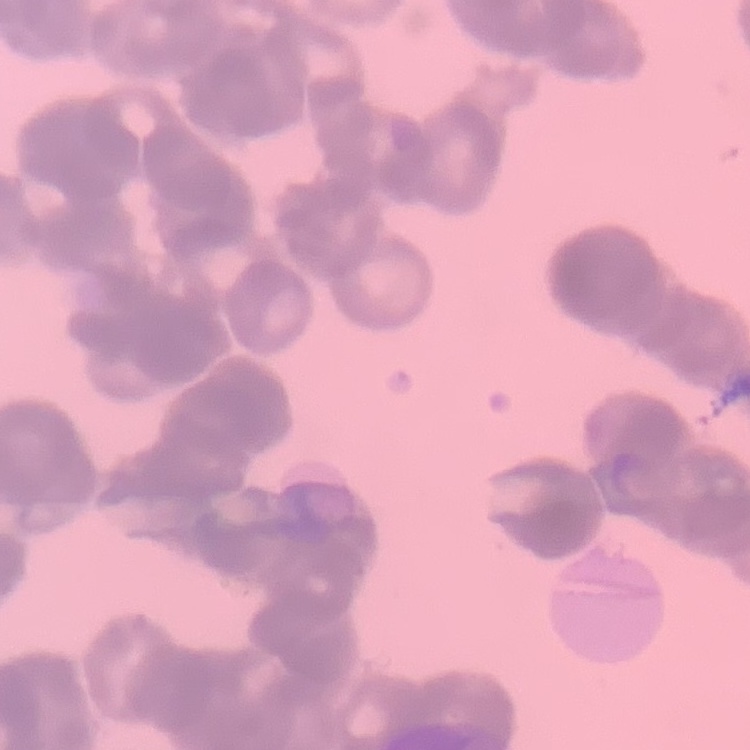

The red blood cells exhibit rouleaux formation. Stained with either Field's or Giemsa. Thin blood film. One tile cut from a larger photomicrograph.